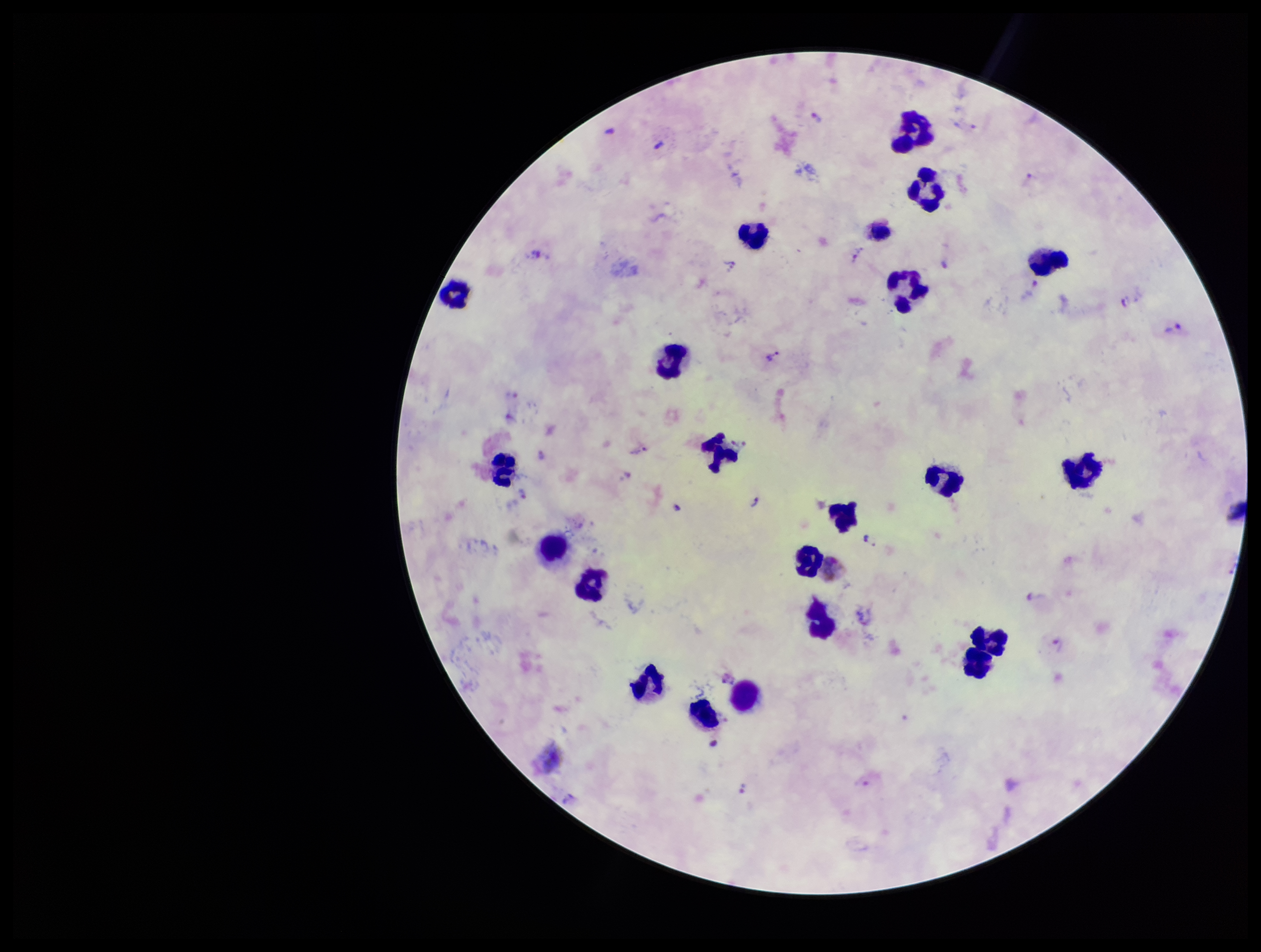

species reported for this patient = Plasmodium vivax
stain = Giemsa
parasite count = 15
capture = smartphone photograph through the microscope eyepiece
preparation = thick
leukocyte count = 21
Plasmodium parasites = seen
patient malaria status = infected
field of view = one from this slide
image size = 1261×952 pixels